Identify the parasite.
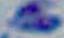

Toxoplasma gondii.

magnification = 1000x
modality = micrograph